Assess the morphology of the red blood cells.
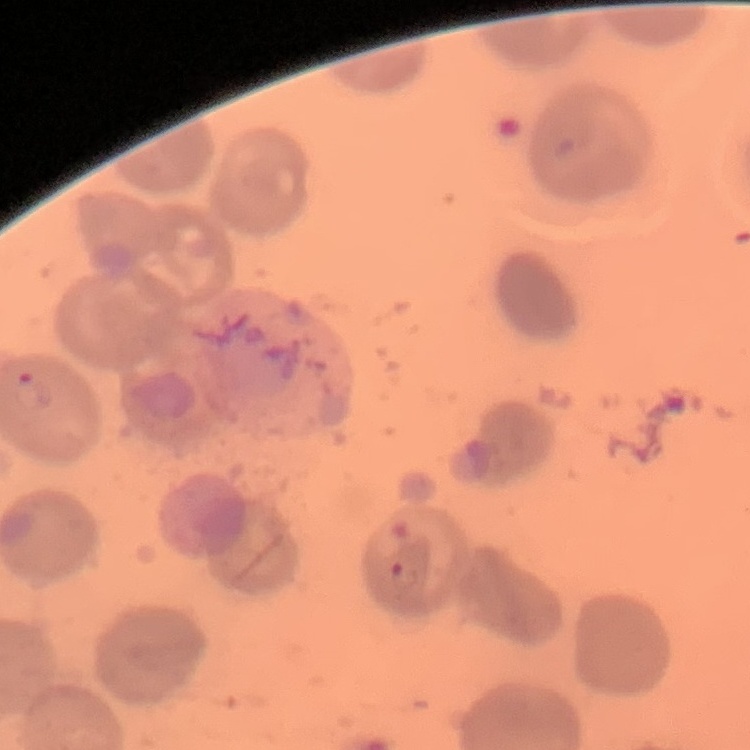

They show no rouleaux formation.

image type = square crop of a larger photomicrograph
stain = Field's or Giemsa
preparation = thin blood smear